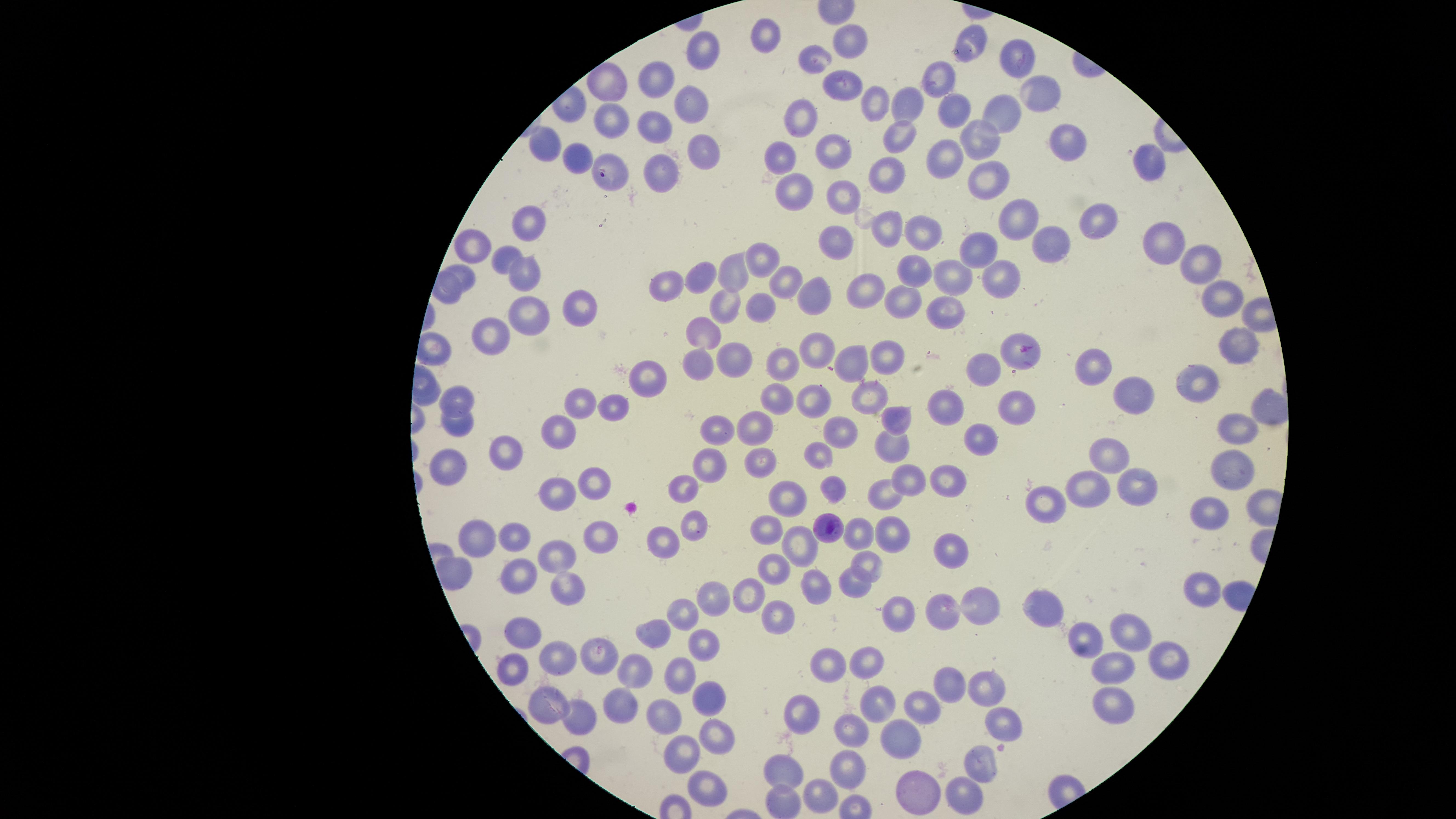

Approximate marker points as [x, y] in pixels. Uninfected red blood cells: [768, 34], [852, 41], [973, 42], [1020, 49], [704, 51], [817, 58], [941, 76], [656, 79], [606, 82], [839, 87], [1035, 88], [687, 98], [878, 101], [951, 105], [910, 106], [994, 106], [805, 111], [1004, 116], [608, 120], [655, 125], [898, 136], [1065, 142], [551, 143], [981, 144], [831, 150], [788, 153], [699, 154], [946, 157], [1143, 158], [578, 159], [660, 171], [887, 173], [980, 175], [793, 191], [842, 197], [1102, 214], [1024, 222], [529, 225], [922, 227], [893, 228], [1057, 239], [837, 240], [477, 243], [1158, 244], [984, 247], [507, 253], [766, 258], [1200, 262], [915, 268], [523, 269], [732, 270], [959, 271], [1005, 271], [701, 274], [465, 277], [788, 277], [674, 283], [872, 291], [814, 295], [1222, 297], [906, 299], [721, 305], [763, 305], [574, 307], [951, 310], [523, 312], [708, 333], [490, 334], [1241, 339], [816, 350], [891, 351], [1019, 355], [856, 356], [736, 362], [699, 364], [1092, 364], [786, 366], [981, 368], [640, 377], [1204, 379], [1131, 391], [871, 395], [775, 396], [820, 397], [459, 399], [577, 404], [952, 405], [1018, 406], [615, 407], [901, 414], [459, 427], [754, 428], [839, 428], [720, 430], [1235, 430], [556, 432], [983, 438], [895, 447], [497, 450], [1112, 454], [819, 456], [758, 463], [1232, 463], [453, 464], [709, 465], [595, 478], [908, 480], [945, 481], [687, 482], [1095, 485], [1139, 487], [830, 488], [881, 492], [557, 493], [789, 500], [1054, 500], [1215, 507], [690, 526], [596, 531], [767, 531], [863, 532], [885, 533], [481, 535], [514, 535], [661, 539], [802, 540], [557, 547], [954, 550], [867, 566], [771, 570], [517, 576], [854, 580], [815, 586], [566, 587], [744, 590], [711, 598], [982, 605], [685, 609], [774, 609], [1053, 609], [944, 611], [901, 614], [654, 633], [1132, 633], [524, 634], [1086, 641], [705, 650], [1170, 654], [598, 656], [560, 661], [831, 662], [520, 665], [870, 665], [636, 666], [1112, 666], [679, 676], [948, 681], [982, 687], [1110, 693], [710, 696], [547, 705], [616, 705], [918, 705], [875, 709], [665, 712], [801, 714], [579, 716], [1005, 724], [715, 733], [849, 733], [901, 736], [683, 756], [977, 764], [850, 766], [785, 770], [707, 780], [921, 788], [959, 790], [822, 792], [781, 800]. Parasitized red blood cells: [609, 170], [826, 526]. Photographed with a smartphone camera through the microscope eyepiece. Species: Plasmodium falciparum. Thin smear of blood. Image is 1456×819 pixels. One field of view of the specimen. The visible region is circular. Presence: malaria parasites identified. Giemsa stain.